Evaluate for Plasmodium parasites.
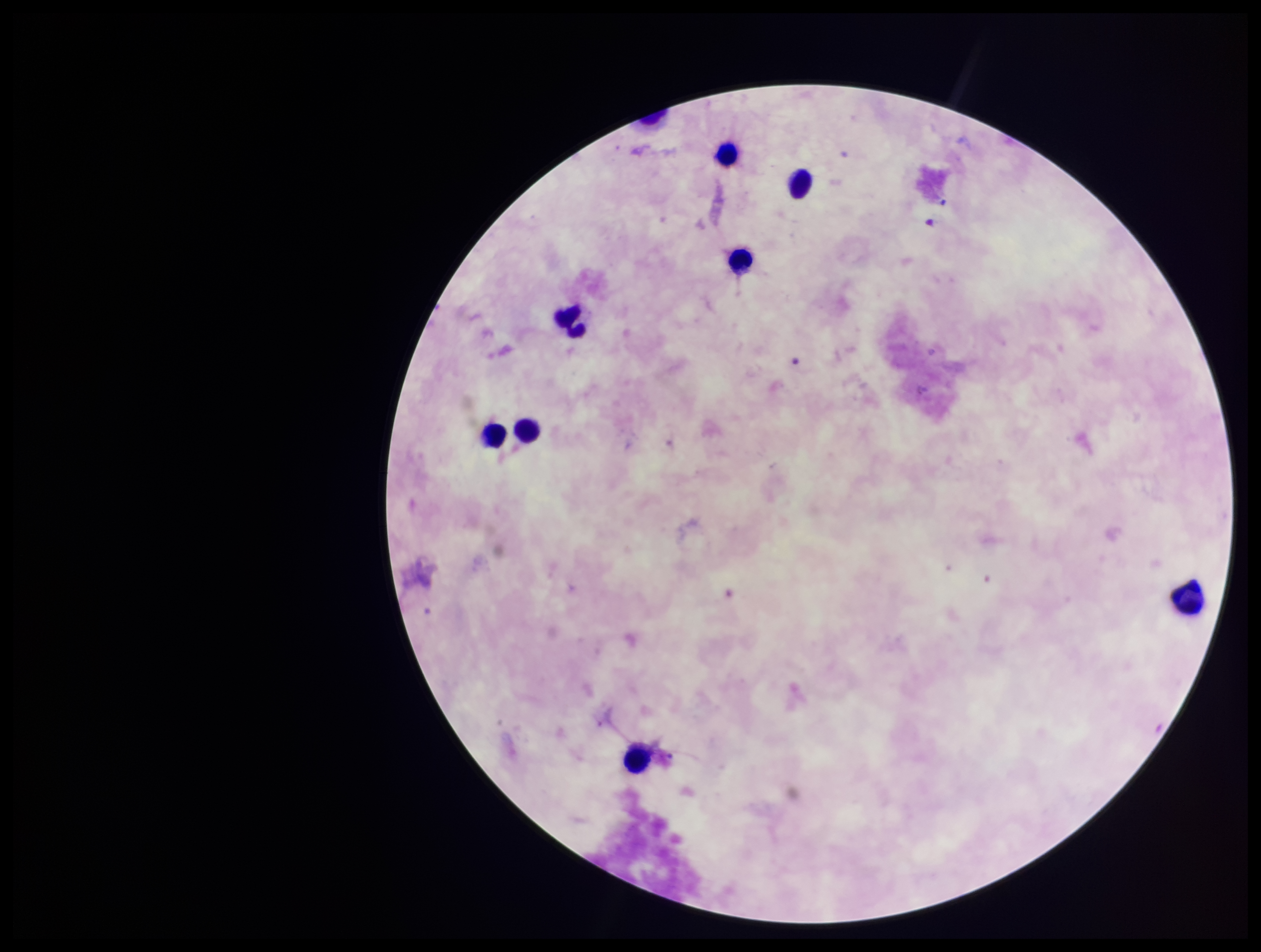
None seen.

Summary:
  - Image size: 1261×952 pixels
  - Stain: Giemsa
  - Capture: smartphone photograph through the microscope eyepiece
  - Leukocyte count: 8
  - Field of view: one from this slide
  - Preparation: thick smear
  - Patient malaria status: negative
  - Parasite count: 0